Locate every leukocyte (white blood cell).
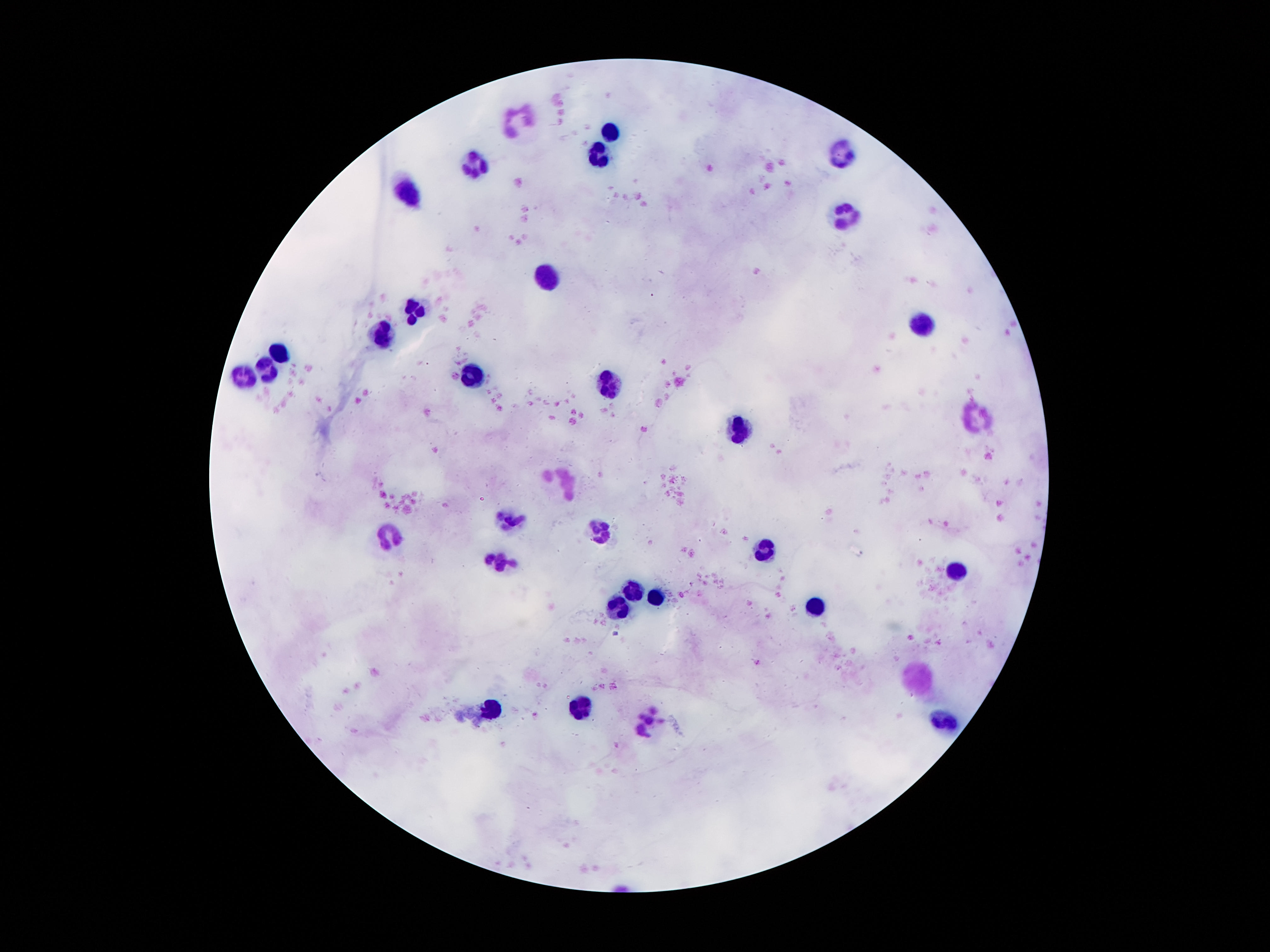

Approximate centers as [x, y] in pixels.
Leukocytes: [517, 117], [611, 132], [598, 154], [839, 154], [475, 163], [407, 192], [845, 215], [544, 280], [417, 309], [921, 324], [384, 335], [278, 353], [269, 368], [476, 373], [247, 378], [606, 385], [972, 419], [740, 433], [568, 483], [509, 519], [598, 531], [391, 539], [766, 549], [498, 562], [956, 572], [633, 592], [654, 597], [816, 607], [616, 608], [919, 676], [582, 707], [491, 709], [651, 719], [944, 723].

{
  "preparation": "thick blood film",
  "capture": "smartphone camera through the microscope eyepiece",
  "field_of_view": "single",
  "image_size": "1270×952 pixels",
  "magnification": "100x",
  "stain": "Giemsa",
  "patient_malaria_status": "negative"
}